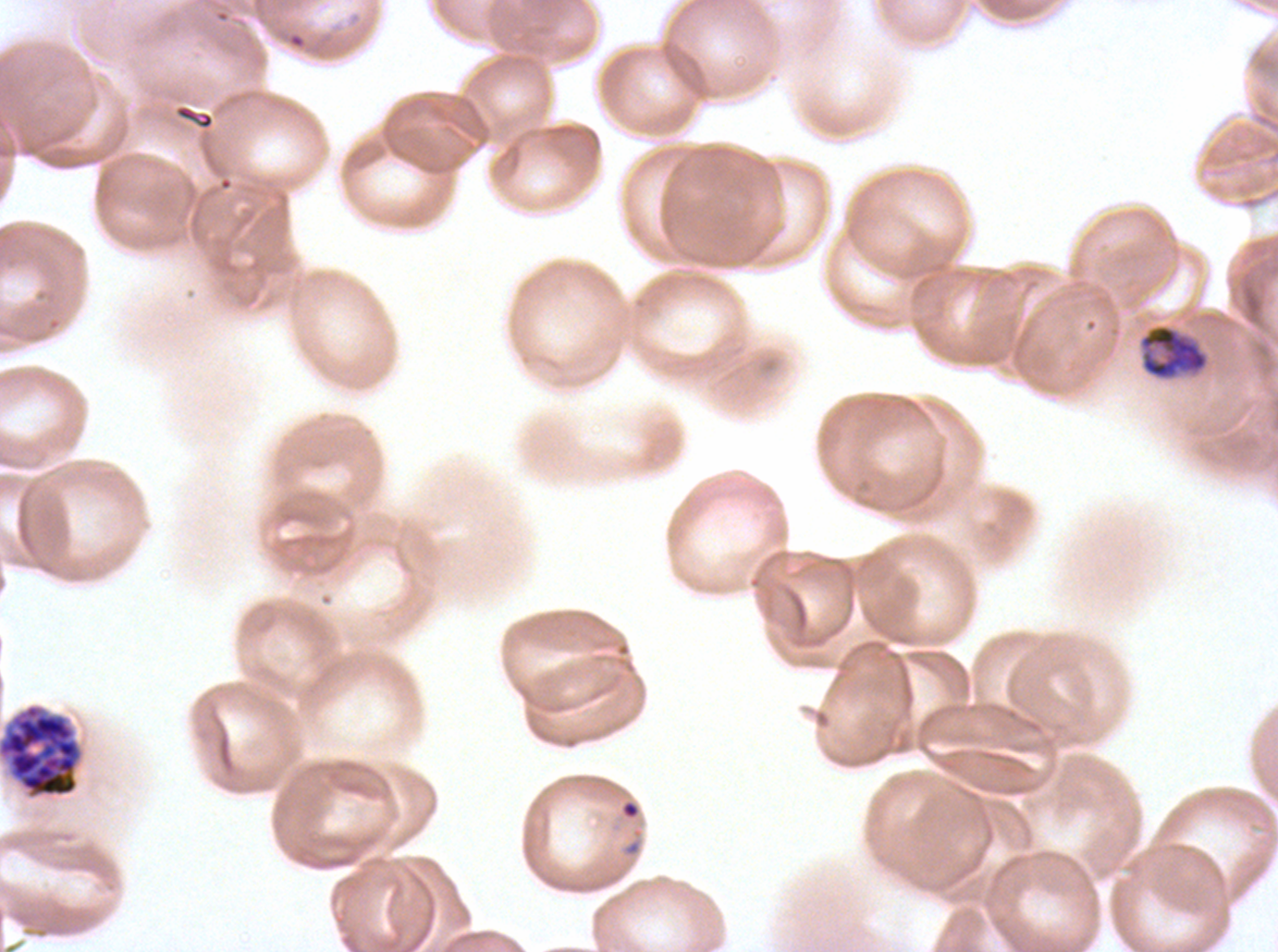

notation = approximate bounding rectangles given as corner coordinates in pixels from the top-left
mid trophozoite locations = (x1=1138, y1=323, x2=1209, y2=380)
late schizont locations = (x1=0, y1=704, x2=81, y2=798)
ring locations = (x1=621, y1=800, x2=639, y2=818)
life-cycle stages observed = ring, mid trophozoite, late schizont
specimen = P. falciparum cultured ex vivo for 24 to 48 hours, from a patient in The Gambia
preparation = thin blood film
image size = 1278×952 pixels
field of view = sub-image separated from a larger composite
stain = Giemsa